Name the cell type shown.
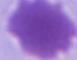

This is an erythrocyte.

modality = micrograph
magnification = 1000x